Report the malaria status of this cell.
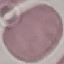

Uninfected.

{
  "stain": "Giemsa",
  "preparation": "thin smear",
  "image_type": "automatically extracted cell patch, resized to 64 × 64 pixels",
  "capture": "smartphone camera at the microscope eyepiece"
}